Name the parasite shown.
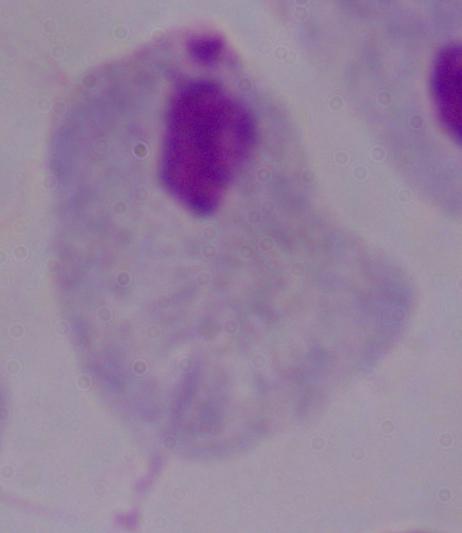

A trichomonad.

Summary:
  - Magnification: 1000x
  - Modality: photomicrograph